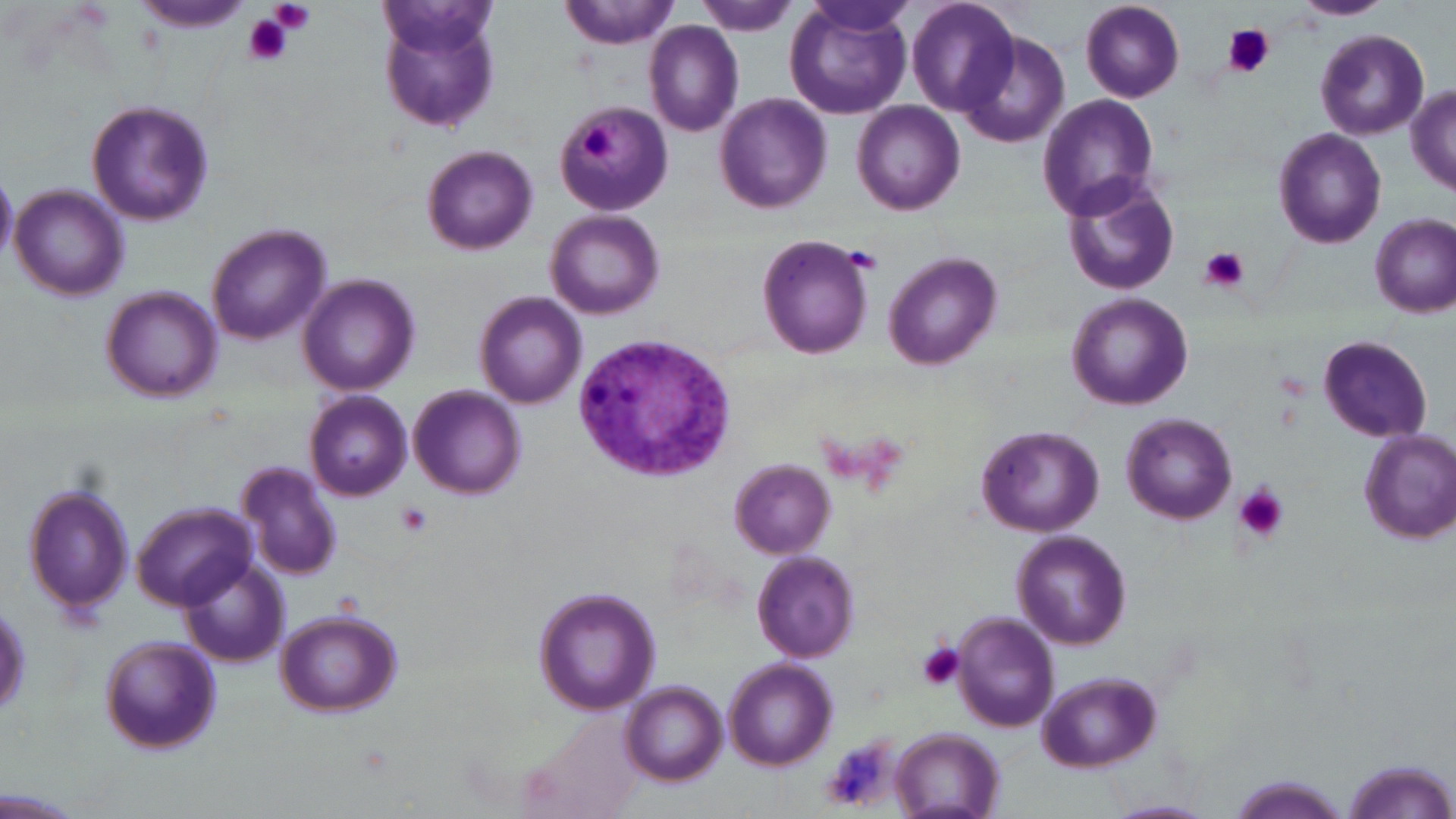

Summary:
  - Coordinate format: approximate bounding boxes as (x1, y1, x2, y2) in pixels
  - Platelet locations: (270, 0, 316, 35), (244, 14, 295, 66), (1223, 25, 1274, 78), (577, 126, 614, 163), (1199, 247, 1248, 293), (1234, 483, 1288, 542), (396, 503, 434, 537), (916, 642, 966, 692), (821, 737, 897, 811)
  - Plasmodium vivax-infected red blood cell locations: (571, 330, 737, 485)
  - Uninfected red blood cell locations: (557, 0, 682, 50), (906, 0, 1020, 116), (1080, 0, 1186, 103), (1295, 0, 1391, 20), (697, 2, 800, 36), (785, 2, 914, 120), (136, 3, 249, 35), (374, 4, 503, 136), (645, 22, 743, 136), (958, 28, 1071, 149), (1317, 29, 1428, 139), (1407, 86, 1456, 195), (1037, 94, 1160, 221), (714, 95, 833, 213), (853, 100, 965, 216), (86, 101, 214, 228), (556, 102, 675, 213), (1273, 128, 1387, 249), (420, 145, 538, 256), (0, 171, 17, 263), (1062, 175, 1181, 296), (10, 184, 128, 299), (546, 209, 666, 320), (1371, 214, 1455, 317), (206, 224, 329, 345), (757, 232, 876, 359), (884, 252, 1002, 369), (299, 275, 419, 396), (102, 288, 222, 400), (475, 292, 586, 408), (1066, 292, 1194, 410), (1316, 334, 1431, 442), (409, 385, 525, 499), (307, 391, 411, 501), (1122, 413, 1237, 523), (977, 426, 1104, 538), (1358, 429, 1456, 546), (729, 460, 835, 558), (238, 462, 345, 580), (23, 479, 136, 618), (134, 503, 254, 612), (1013, 531, 1132, 653), (753, 549, 863, 661), (179, 558, 289, 670), (533, 587, 661, 717), (273, 609, 401, 718), (953, 614, 1059, 732), (98, 635, 222, 757), (724, 659, 836, 769), (1038, 673, 1163, 772), (621, 681, 727, 784), (891, 729, 1004, 818), (1340, 758, 1454, 819), (1228, 777, 1349, 818), (1105, 799, 1213, 819)
  - Slide-level diagnosis: Plasmodium vivax
  - Field of view: single
  - Magnification: 1000x
  - Stain: May-Grünwald-Giemsa
  - Image size: 1456×819 pixels
  - Modality: light microscopy
  - Preparation: thin blood film